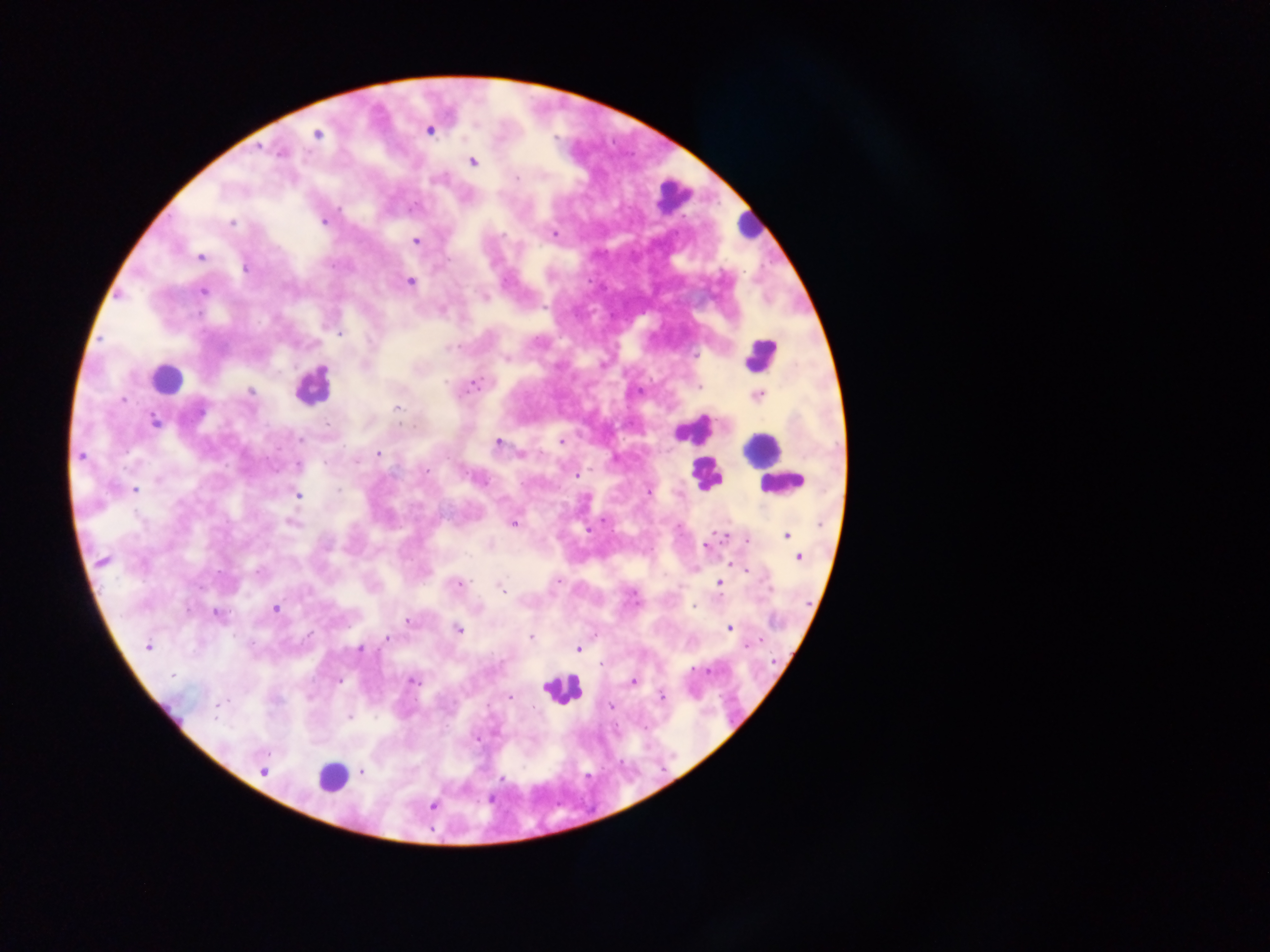
field of view = single
image size = 1270×952 pixels
malaria parasite locations = approximate centers as [x, y] in pixels: [430, 130], [318, 134], [259, 147], [281, 152], [473, 162], [516, 178], [339, 208], [231, 222], [323, 222], [555, 233], [416, 240], [201, 257], [245, 269], [410, 281], [203, 292], [484, 297], [340, 334], [451, 348], [506, 358], [602, 364], [446, 382], [474, 385], [699, 387], [250, 392], [758, 396], [124, 400], [397, 407], [154, 421], [300, 438], [562, 442], [497, 443], [378, 453], [521, 454], [80, 456], [355, 461], [299, 464], [426, 469], [576, 475], [134, 490], [339, 490], [649, 492], [298, 495], [292, 524], [513, 524], [726, 535], [786, 535], [748, 541], [705, 545], [798, 558], [102, 561], [731, 563], [257, 571], [557, 581], [719, 583], [459, 584], [500, 587], [693, 605], [276, 609], [217, 613], [408, 620], [730, 628], [458, 629], [530, 637], [388, 639], [147, 647], [360, 649], [578, 649], [601, 664], [173, 675], [340, 681], [413, 682], [633, 682], [510, 698], [661, 698], [218, 705], [610, 706], [349, 717], [477, 739], [266, 753], [262, 771], [362, 771], [502, 778], [432, 806]
preparation = thick blood film
leukocyte locations = approximate centers as [x, y] in pixels: [672, 196], [748, 227], [760, 354], [167, 377], [310, 386], [698, 428], [763, 449], [706, 473], [780, 484], [562, 691], [331, 776]
capture = mobile-phone photograph through a microscope
country = Ghana